Classify this cell by malaria status.
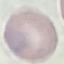

It is uninfected.

image type = automatically extracted cell patch, resized to 64 × 64 pixels
capture = smartphone camera at the microscope eyepiece
preparation = thin smear
stain = Giemsa